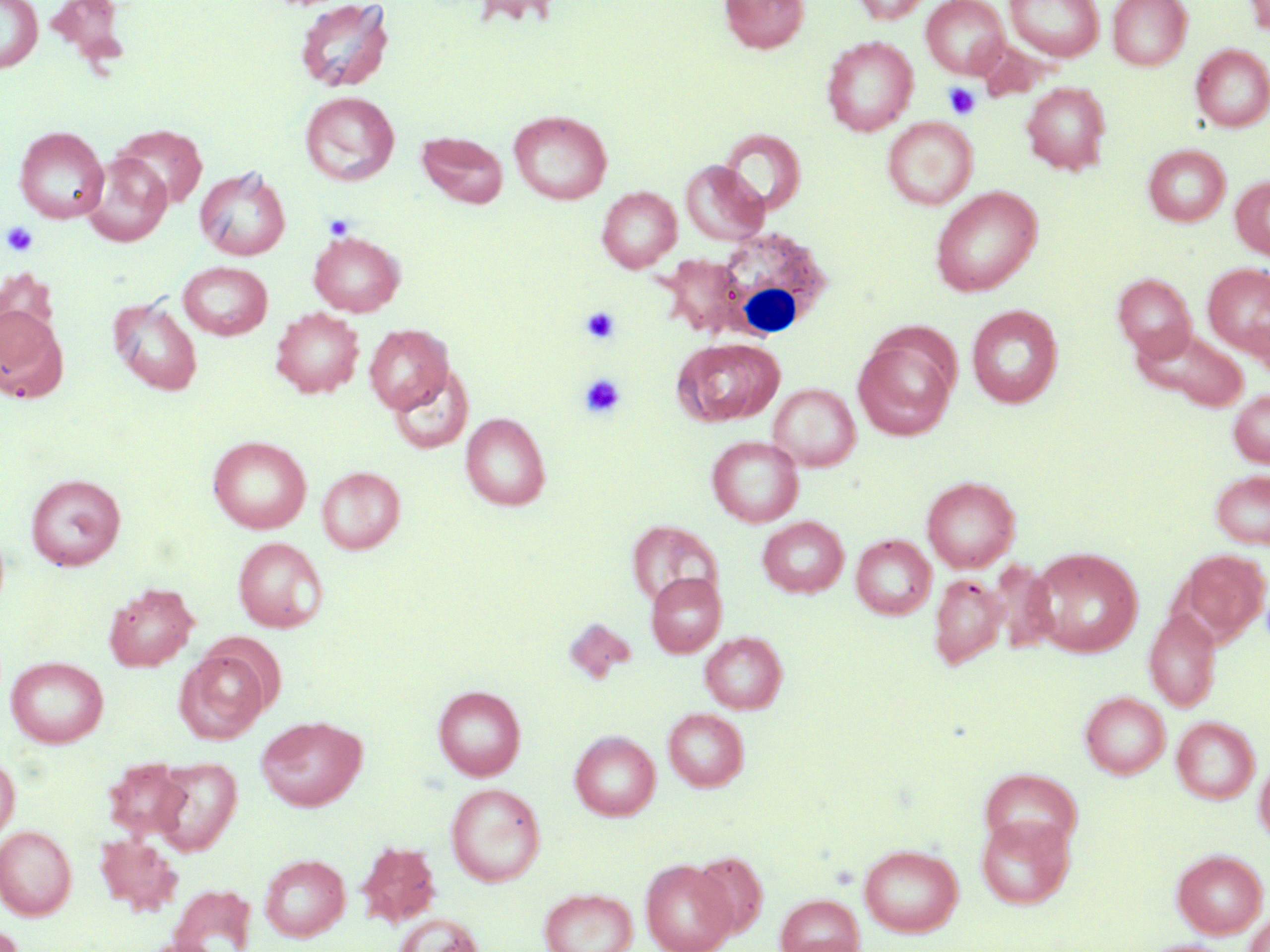

slide_level_diagnosis: negative for blood parasites
uninfected_red_blood_cell_locations: 'approximate bounding boxes as (x1,y1)-(x2,y2) corner pairs in pixels: (0,0)-(42,72), (47,0)-(129,61), (295,0)-(393,93), (471,0)-(562,30), (720,0)-(810,53), (852,0)-(932,24), (921,0)-(1009,78), (1005,0)-(1104,61), (1108,0)-(1192,70), (1245,0)-(1270,39), (822,36)-(917,135), (974,39)-(1051,102), (1191,44)-(1270,132), (1022,83)-(1111,174), (300,91)-(399,185), (509,110)-(612,204), (882,117)-(978,210), (111,123)-(207,211), (14,126)-(108,223), (720,130)-(806,216), (417,131)-(508,208), (1144,144)-(1230,226), (81,153)-(172,246), (680,161)-(768,245), (195,167)-(291,260), (1231,176)-(1270,260), (597,186)-(682,271), (930,186)-(1042,296), (309,231)-(405,316), (658,256)-(749,336), (178,261)-(273,339), (1202,263)-(1270,357), (1113,273)-(1196,360), (109,295)-(202,395), (0,305)-(67,402), (967,305)-(1063,407), (271,308)-(364,398), (365,324)-(453,413), (1133,326)-(1248,411), (853,334)-(957,439), (673,337)-(784,427), (389,366)-(473,454), (768,383)-(860,471), (1228,389)-(1270,467), (461,413)-(551,510), (208,436)-(312,533), (707,436)-(804,527), (317,466)-(405,554), (1210,469)-(1270,549), (25,474)-(126,570), (922,476)-(1020,572), (757,516)-(848,597), (627,519)-(723,612), (852,534)-(936,619), (232,536)-(328,632), (1028,548)-(1143,657), (1177,549)-(1269,644), (646,572)-(726,657), (929,574)-(1008,669), (104,582)-(198,672), (1145,608)-(1221,712), (700,631)-(787,713), (175,650)-(268,744), (6,656)-(109,748), (434,684)-(526,780), (1079,691)-(1171,778), (663,708)-(749,791), (256,715)-(367,811), (1172,716)-(1260,804), (570,730)-(661,820), (0,753)-(20,841), (1255,753)-(1270,845), (151,756)-(242,856), (106,758)-(192,839), (446,783)-(545,886), (976,812)-(1076,911), (0,825)-(77,920), (95,833)-(183,915), (355,839)-(443,929), (859,844)-(963,937), (1171,849)-(1268,938), (691,851)-(767,937), (260,854)-(350,941), (641,858)-(736,952), (169,884)-(257,952), (539,887)-(638,952), (775,894)-(865,952), (1243,909)-(1270,951), (393,913)-(483,952), (137,937)-(227,952), (1138,939)-(1236,952)'
platelet_locations: 'approximate bounding boxes as (x1,y1)-(x2,y2) corner pairs in pixels: (944,83)-(981,120), (324,215)-(356,241), (2,221)-(39,257), (580,306)-(622,345), (580,374)-(626,419)'
modality: light microscopy
magnification: 1000x
field_of_view: single
preparation: thin blood smear
image_size: 1270×952 pixels
white_blood_cell_locations: 'approximate bounding boxes as (x1,y1)-(x2,y2) corner pairs in pixels: (709,226)-(832,343)'
stain: May-Grünwald-Giemsa